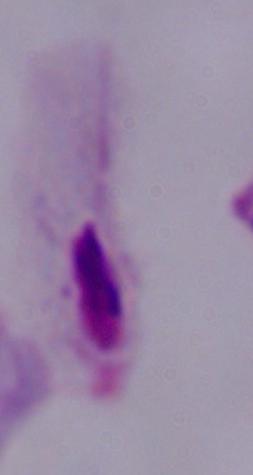

Summary:
  - Identification: trichomonad
  - Magnification: 1000x
  - Modality: micrograph